Describe the morphology of the erythrocytes.
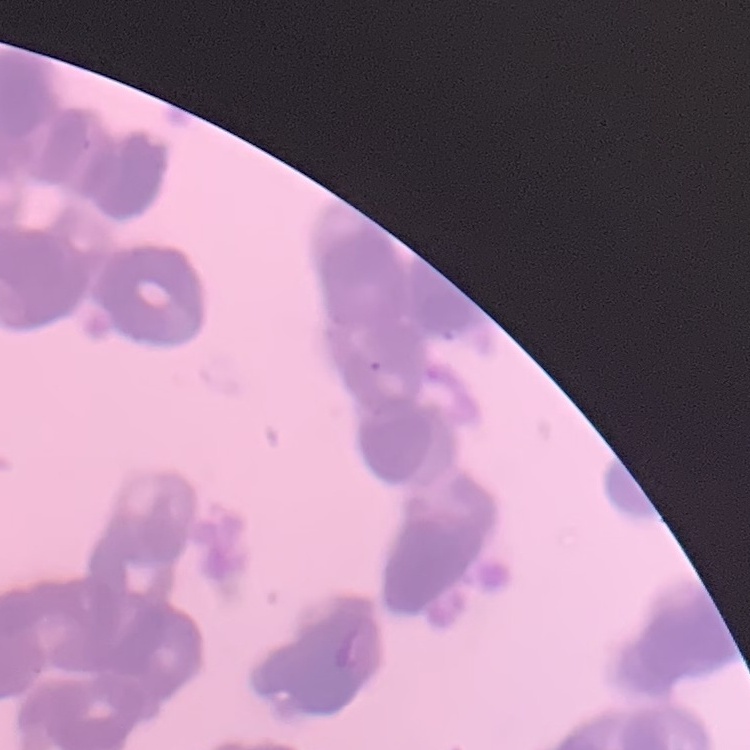

They show rouleaux formation.

Summary:
  - Preparation: thin blood film
  - Image type: one tile cut from a larger photomicrograph
  - Stain: Field's or Giemsa